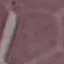
Summary:
  - Malaria status: uninfected
  - Stain: Giemsa
  - Capture: smartphone through the microscope eyepiece
  - Preparation: thin blood smear
  - Image type: cell patch, automatically extracted from a larger field of view and resized to 64 × 64 pixels